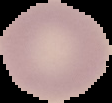

Image is 112×103 pixels. The area outside the segmented cell region is set to black. Malaria status: uninfected. From a thin blood film.